Assess this cell for malaria.
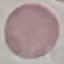
It is uninfected.

Summary:
  - Preparation: thin blood film
  - Image type: automatically extracted cell patch, resized to 64 × 64 pixels
  - Capture: smartphone camera at the microscope eyepiece
  - Stain: Giemsa